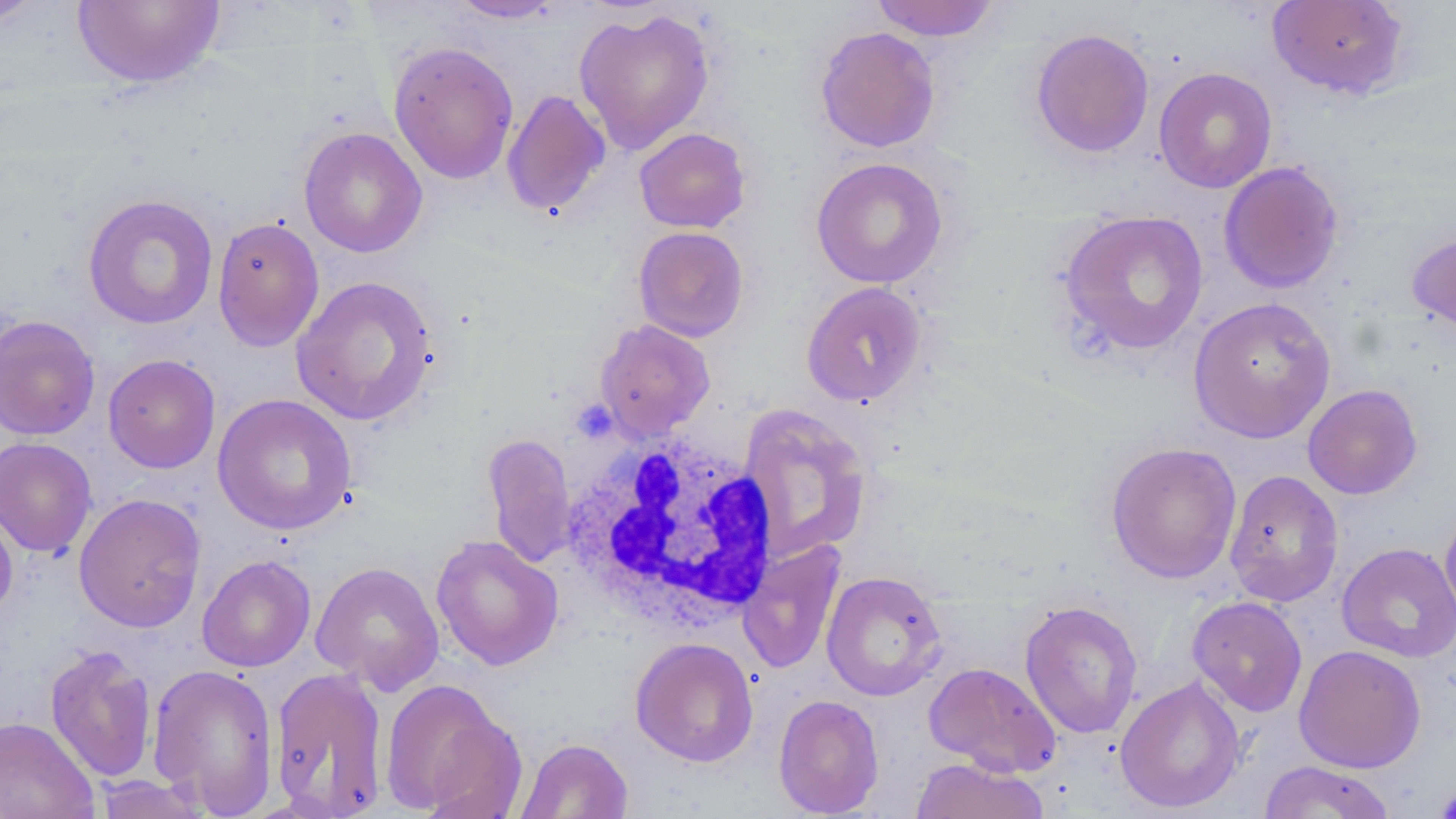
Approximate bounding boxes as named x1/y1/x2/y2 corners in pixels. White blood cell locations: (x1=561, y1=428, x2=779, y2=632). Uninfected red blood cell locations: (x1=0, y1=0, x2=46, y2=29), (x1=73, y1=0, x2=224, y2=89), (x1=448, y1=0, x2=567, y2=23), (x1=870, y1=0, x2=999, y2=42), (x1=1267, y1=0, x2=1409, y2=100), (x1=574, y1=8, x2=715, y2=155), (x1=814, y1=26, x2=941, y2=153), (x1=1030, y1=28, x2=1154, y2=158), (x1=388, y1=41, x2=520, y2=184), (x1=1153, y1=67, x2=1277, y2=193), (x1=502, y1=89, x2=611, y2=217), (x1=298, y1=126, x2=428, y2=258), (x1=634, y1=127, x2=751, y2=233), (x1=811, y1=157, x2=948, y2=289), (x1=1218, y1=161, x2=1344, y2=294), (x1=83, y1=193, x2=219, y2=330), (x1=1057, y1=210, x2=1209, y2=357), (x1=212, y1=217, x2=325, y2=351), (x1=633, y1=226, x2=749, y2=342), (x1=1408, y1=228, x2=1456, y2=338), (x1=291, y1=275, x2=439, y2=426), (x1=801, y1=281, x2=928, y2=407), (x1=1188, y1=296, x2=1336, y2=443), (x1=0, y1=315, x2=100, y2=441), (x1=594, y1=319, x2=715, y2=440), (x1=103, y1=353, x2=220, y2=473), (x1=1302, y1=384, x2=1422, y2=499), (x1=212, y1=393, x2=357, y2=536), (x1=738, y1=404, x2=873, y2=562), (x1=483, y1=433, x2=577, y2=568), (x1=0, y1=437, x2=97, y2=559), (x1=1105, y1=441, x2=1242, y2=584), (x1=1224, y1=469, x2=1344, y2=607), (x1=73, y1=492, x2=206, y2=632), (x1=0, y1=500, x2=18, y2=622), (x1=1439, y1=504, x2=1456, y2=628), (x1=430, y1=534, x2=564, y2=671), (x1=737, y1=539, x2=846, y2=674), (x1=1336, y1=542, x2=1456, y2=663), (x1=197, y1=554, x2=316, y2=672), (x1=310, y1=561, x2=445, y2=694), (x1=821, y1=570, x2=948, y2=701), (x1=1187, y1=596, x2=1308, y2=717), (x1=1019, y1=600, x2=1143, y2=739), (x1=630, y1=637, x2=759, y2=767), (x1=44, y1=643, x2=158, y2=784), (x1=1294, y1=644, x2=1426, y2=773), (x1=923, y1=661, x2=1062, y2=777), (x1=147, y1=663, x2=280, y2=817), (x1=270, y1=667, x2=389, y2=817), (x1=1115, y1=675, x2=1246, y2=813), (x1=379, y1=677, x2=519, y2=817), (x1=772, y1=694, x2=885, y2=818), (x1=0, y1=715, x2=98, y2=819), (x1=515, y1=737, x2=634, y2=819), (x1=909, y1=757, x2=1051, y2=819), (x1=1258, y1=761, x2=1397, y2=818), (x1=92, y1=774, x2=211, y2=818), (x1=1434, y1=780, x2=1456, y2=818). Platelet locations: (x1=1063, y1=314, x2=1119, y2=363), (x1=574, y1=393, x2=617, y2=443), (x1=1434, y1=782, x2=1456, y2=818). Slide-level diagnosis: negative for blood parasites. May-Grünwald-Giemsa stain. Thin blood smear. One field of a larger specimen. Image is 1456×819 pixels. Light microscopy. 1000x magnification.